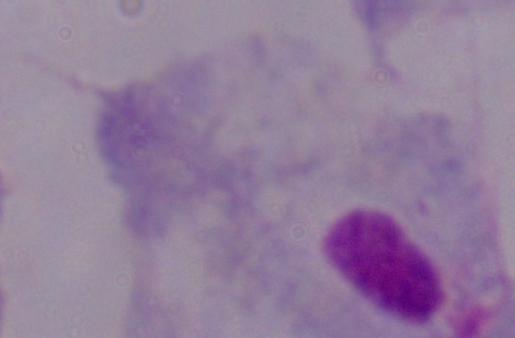

magnification = 1000x
modality = photomicrograph
identification = trichomonad